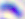

Summary:
  - Identification: Toxoplasma gondii
  - Magnification: 400x
  - Modality: micrograph